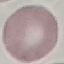
{
  "result": "no malaria parasites seen",
  "capture": "smartphone camera at the microscope eyepiece",
  "stain": "Giemsa",
  "preparation": "thin blood smear",
  "image_type": "cell patch, automatically extracted from a larger field of view and resized to 64 × 64 pixels"
}